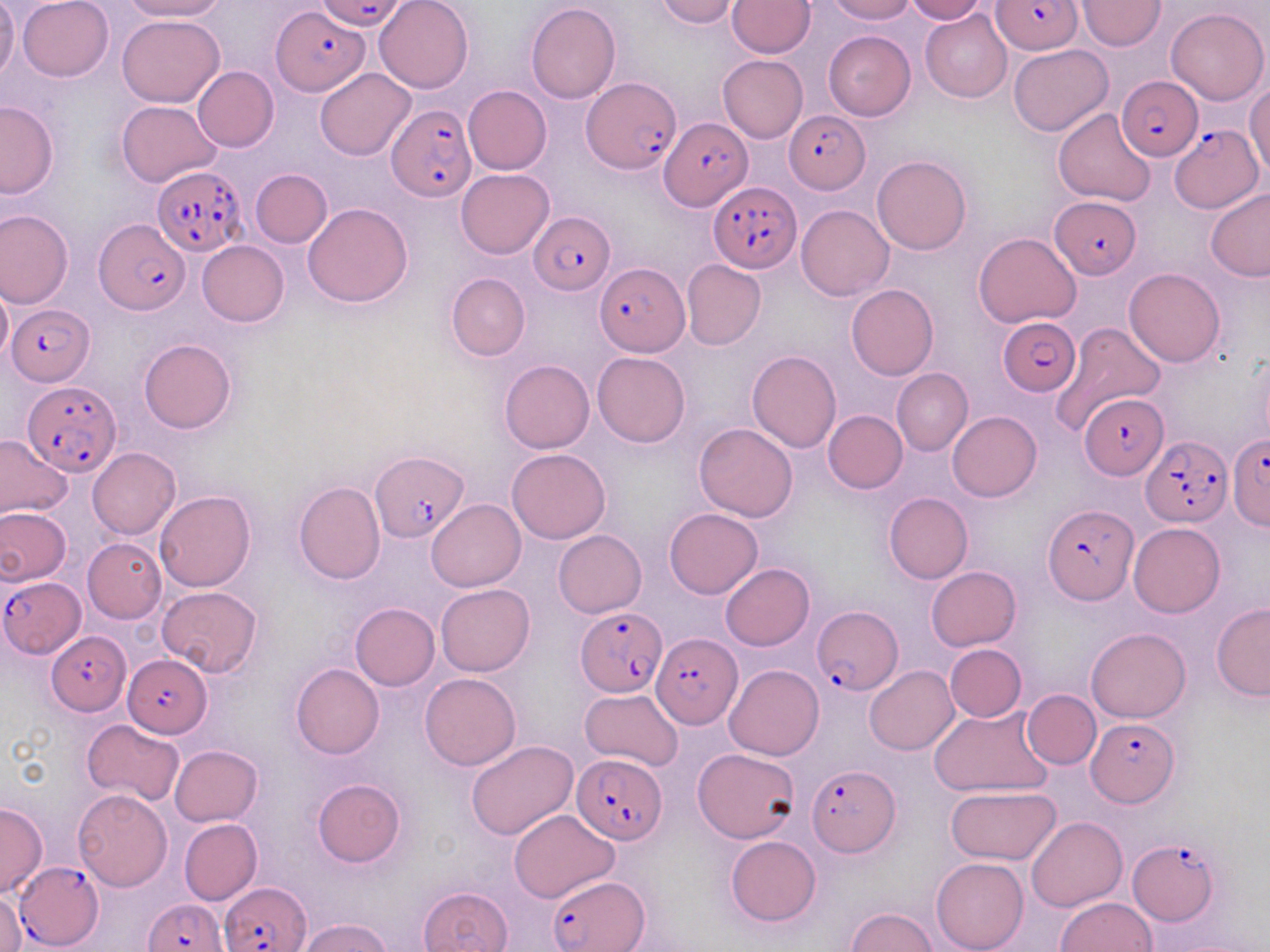
slide-level diagnosis = Plasmodium falciparum
magnification = 1000x
Plasmodium falciparum-infected red blood cell locations = approximate bounding boxes as (x1,y1)-(x2,y2) corner pairs in pixels: (317,0)-(409,30), (993,0)-(1082,56), (273,9)-(369,96), (582,76)-(680,173), (1117,76)-(1202,160), (389,102)-(476,203), (784,110)-(870,193), (656,118)-(749,211), (1168,125)-(1263,213), (153,166)-(246,255), (708,182)-(802,272), (1050,195)-(1140,278), (528,210)-(615,294), (94,218)-(190,315), (595,262)-(689,356), (8,302)-(94,383), (996,315)-(1075,398), (22,380)-(120,476), (1082,393)-(1166,479), (1229,434)-(1270,530), (1140,437)-(1230,526), (371,451)-(469,540), (1042,503)-(1138,604), (1,575)-(85,658), (810,605)-(902,697), (575,607)-(667,697), (46,631)-(129,714), (650,633)-(740,727), (124,654)-(212,736), (1088,717)-(1179,806), (574,754)-(667,845), (806,765)-(900,855), (1128,837)-(1221,926), (12,862)-(103,948), (546,876)-(648,951), (221,881)-(313,951), (145,899)-(228,952)
modality = light microscopy
stain = May-Grünwald-Giemsa
field of view = single
image size = 1270×952 pixels
preparation = thin blood smear
uninfected red blood cell locations = approximate bounding boxes as (x1,y1)-(x2,y2) corner pairs in pixels: (0,0)-(19,80), (18,0)-(113,82), (123,0)-(228,21), (373,0)-(472,93), (654,0)-(739,26), (728,0)-(814,57), (826,0)-(915,23), (904,0)-(986,23), (1077,0)-(1165,51), (527,3)-(621,103), (1167,6)-(1268,105), (920,9)-(1012,102), (117,14)-(225,106), (823,30)-(915,120), (1008,44)-(1112,136), (718,56)-(807,142), (192,66)-(279,152), (315,68)-(416,161), (1246,84)-(1270,180), (463,85)-(551,175), (117,100)-(221,186), (0,101)-(59,198), (1053,107)-(1157,205), (872,155)-(971,254), (250,169)-(332,247), (456,169)-(553,258), (1205,187)-(1270,280), (303,203)-(413,308), (795,204)-(893,300), (0,210)-(74,308), (973,233)-(1079,329), (196,240)-(288,326), (682,260)-(766,350), (1124,267)-(1225,365), (446,272)-(529,360), (846,283)-(938,379), (0,287)-(12,365), (1050,322)-(1164,434), (139,338)-(236,434), (747,349)-(841,452), (593,352)-(689,447), (499,359)-(595,453), (891,369)-(973,455), (822,410)-(908,493), (947,411)-(1042,501), (693,423)-(799,522), (0,436)-(73,519), (88,448)-(180,539), (506,449)-(612,544), (293,481)-(386,584), (155,490)-(255,591), (883,492)-(972,584), (427,499)-(525,591), (0,506)-(72,585), (665,508)-(762,598), (1129,522)-(1225,616), (554,530)-(646,617), (82,537)-(167,623), (720,563)-(814,651), (925,566)-(1021,651), (435,584)-(535,676), (156,586)-(264,675), (350,602)-(440,690), (1211,603)-(1270,701), (1086,628)-(1190,723), (944,644)-(1026,722), (290,663)-(384,759), (724,664)-(824,760), (864,666)-(959,754), (419,673)-(521,770), (579,689)-(683,770), (1022,690)-(1101,768), (928,708)-(1052,798), (81,718)-(186,806), (466,740)-(578,840), (169,745)-(263,827), (693,748)-(800,843), (313,778)-(406,867), (945,786)-(1061,865), (72,788)-(172,890), (0,802)-(47,899), (508,808)-(620,902), (1026,816)-(1126,912), (178,818)-(262,906), (724,836)-(822,927), (931,857)-(1028,952), (419,886)-(512,952), (1,890)-(25,952), (1056,896)-(1155,951), (845,907)-(938,952), (299,917)-(391,952)